Name the cell type shown.
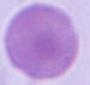

This is an erythrocyte.

modality = photomicrograph
magnification = 1000x